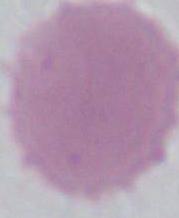
identification = erythrocyte
magnification = 1000x
modality = photomicrograph